Classify this cell by malaria status.
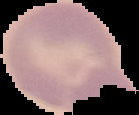
It is uninfected.

From a thin blood smear. Image is 139×115 pixels. Cell region segmented out of the field of view; the surrounding area is masked to black.